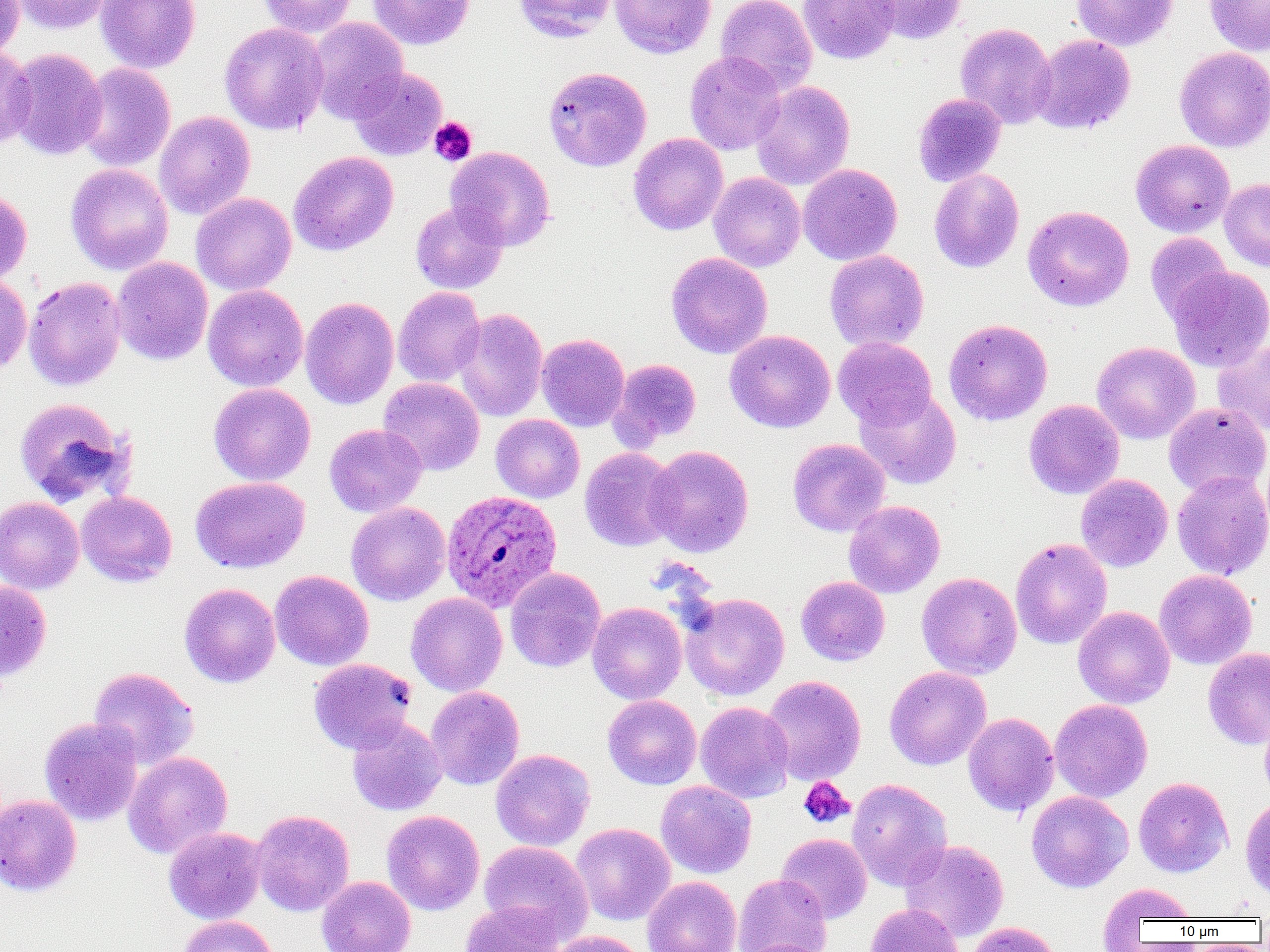
slide-level diagnosis = Plasmodium ovale
uninfected red blood cell locations = approximate bounding boxes as [x1, y1, x2, y2] in pixels: [0, 0, 25, 60], [12, 0, 111, 34], [95, 0, 201, 73], [257, 0, 358, 37], [367, 0, 475, 50], [513, 0, 616, 43], [610, 0, 716, 59], [716, 0, 817, 95], [798, 0, 899, 64], [865, 0, 967, 45], [1072, 0, 1177, 51], [1205, 0, 1270, 56], [308, 17, 408, 124], [219, 22, 328, 135], [956, 23, 1056, 128], [1031, 34, 1136, 134], [0, 44, 36, 152], [1174, 47, 1270, 152], [6, 48, 107, 160], [685, 51, 786, 155], [76, 62, 176, 172], [543, 66, 652, 171], [349, 67, 447, 160], [751, 80, 855, 190], [913, 93, 1006, 187], [154, 111, 255, 220], [628, 133, 728, 235], [1131, 139, 1235, 237], [446, 146, 555, 251], [289, 151, 398, 255], [66, 162, 173, 275], [798, 163, 902, 265], [928, 169, 1025, 273], [708, 172, 806, 272], [1219, 178, 1270, 272], [0, 190, 32, 287], [190, 193, 296, 295], [410, 200, 508, 295], [1023, 205, 1134, 311], [1145, 232, 1234, 327], [824, 250, 929, 352], [666, 252, 772, 358], [112, 257, 213, 365], [1167, 266, 1270, 372], [0, 274, 32, 376], [23, 276, 126, 391], [203, 284, 308, 391], [393, 287, 486, 387], [300, 297, 399, 409], [452, 308, 548, 421], [944, 318, 1053, 425], [725, 330, 835, 433], [537, 333, 630, 431], [833, 336, 937, 429], [1212, 340, 1270, 436], [1091, 341, 1200, 444], [610, 358, 702, 449], [378, 377, 484, 475], [208, 383, 315, 485], [856, 389, 962, 489], [14, 397, 131, 508], [1024, 399, 1124, 500], [1163, 402, 1269, 496], [491, 414, 585, 503], [324, 424, 427, 517], [787, 438, 890, 537], [645, 445, 754, 557], [579, 447, 680, 551], [1171, 470, 1270, 580], [1076, 474, 1173, 571], [190, 476, 310, 573], [76, 491, 178, 587], [0, 496, 84, 594], [844, 500, 945, 598], [346, 502, 451, 606], [1010, 538, 1112, 649], [505, 567, 606, 673], [1155, 569, 1257, 669], [270, 570, 373, 670], [917, 572, 1022, 679], [796, 576, 890, 666], [0, 581, 52, 683], [179, 583, 280, 687], [406, 593, 507, 696], [681, 593, 790, 701], [587, 602, 687, 704], [1073, 606, 1174, 708], [1203, 647, 1270, 749], [308, 658, 417, 754], [884, 666, 991, 770], [88, 667, 198, 769], [762, 675, 866, 786], [426, 687, 525, 790], [602, 694, 702, 790], [1050, 699, 1153, 802], [695, 701, 794, 803], [1259, 710, 1270, 805], [963, 712, 1059, 816], [39, 717, 142, 826], [346, 718, 446, 816], [490, 749, 595, 850], [123, 751, 232, 859], [1133, 777, 1233, 878], [847, 779, 952, 891], [656, 780, 757, 879], [1027, 791, 1133, 892], [0, 793, 82, 896], [1240, 797, 1270, 901], [251, 809, 354, 916], [382, 810, 484, 915], [570, 823, 675, 925], [164, 827, 266, 924], [776, 833, 872, 923], [901, 839, 1009, 942], [479, 841, 593, 942], [733, 874, 832, 952], [317, 876, 416, 952], [642, 876, 741, 952], [1098, 882, 1198, 937], [459, 900, 562, 952], [864, 903, 965, 952], [177, 915, 279, 952], [967, 921, 1061, 952], [543, 930, 649, 952]
magnification = 1000x
modality = light microscopy
preparation = thin blood smear
platelet locations = approximate bounding boxes as [x1, y1, x2, y2] in pixels: [428, 117, 477, 166], [798, 777, 854, 828]
field of view = single
Plasmodium ovale-infected red blood cell locations = approximate bounding boxes as [x1, y1, x2, y2] in pixels: [441, 489, 562, 612]
image size = 1270×952 pixels